Point out Plasmodium parasites and leukocytes.
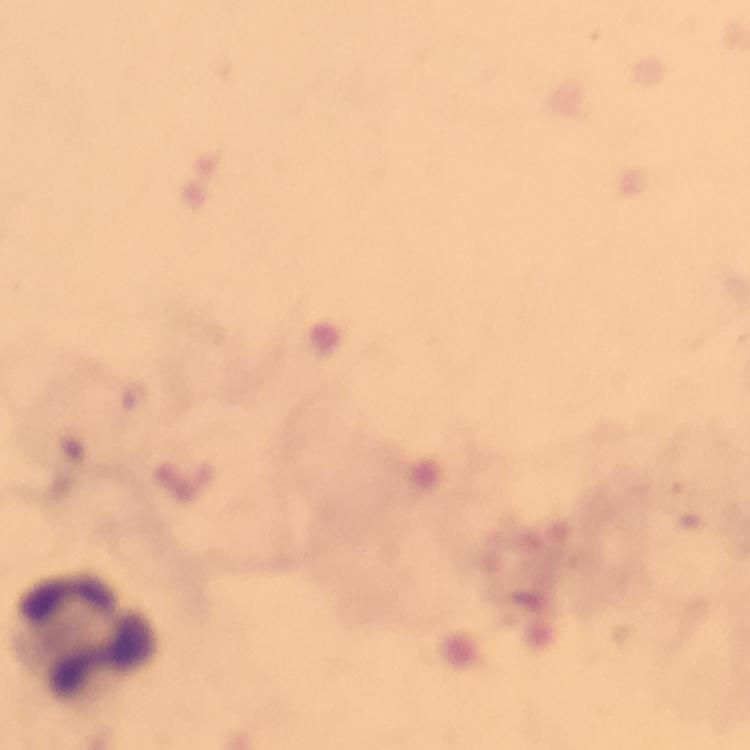

No Plasmodium parasites detected.
Approximate centers as (x, y) in pixels.
Leukocytes: (89, 638).

{
  "capture": "smartphone mounted on the microscope",
  "preparation": "thick smear",
  "stain": "Giemsa",
  "immersion_oil": "applied",
  "magnification": "100x",
  "cropped_from": "one field of view",
  "image_size": "750×750 pixels",
  "context": "from a diagnostic examination for malaria"
}